Name the parasite shown.
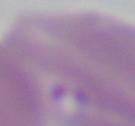

Babesia.

Micrograph. 1000x magnification.